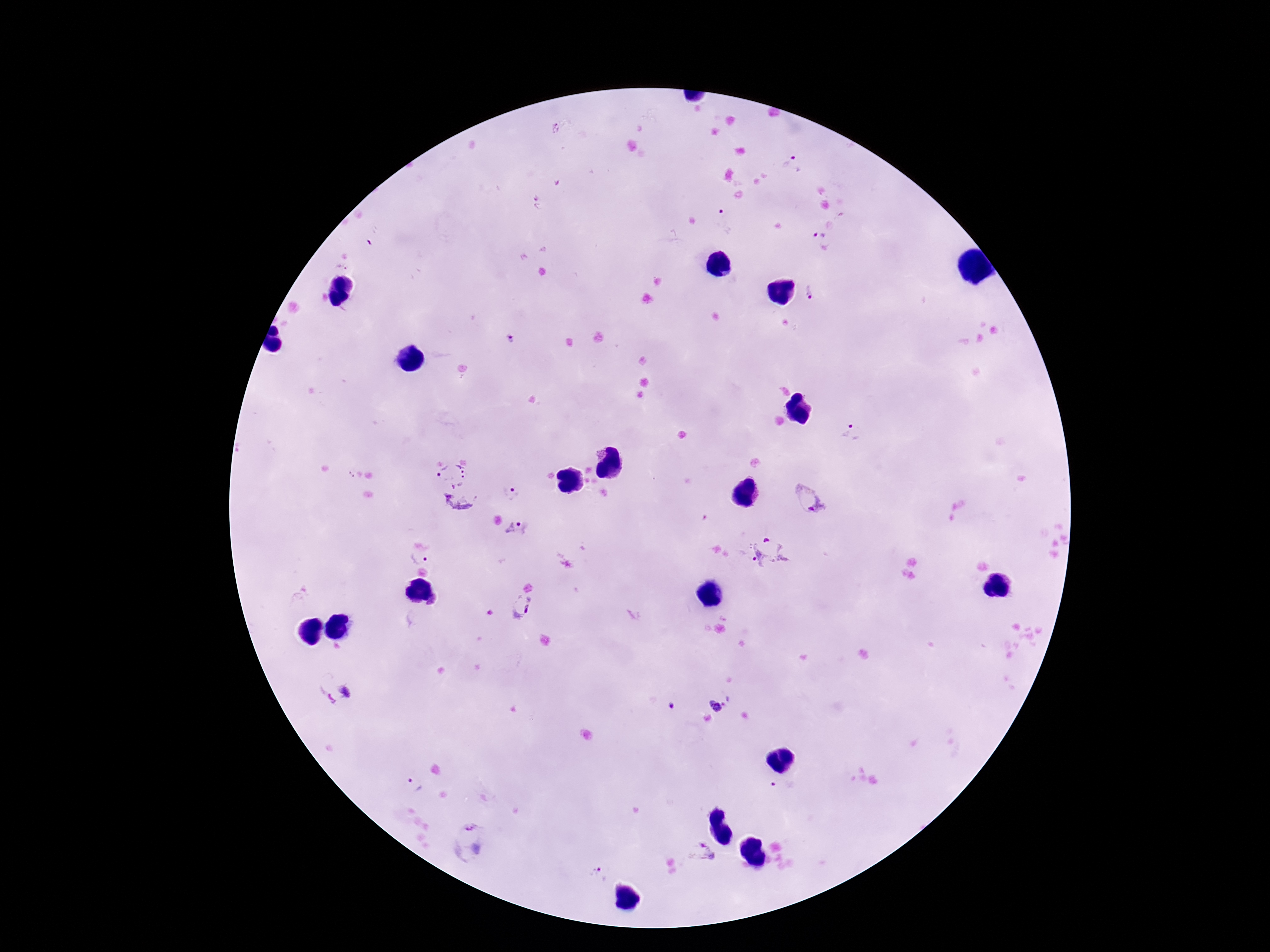
patient malaria status = positive
image size = 1270×952 pixels
magnification = 100x
field of view = single
stain = Giemsa
capture = smartphone camera through the microscope eyepiece
Plasmodium parasite locations = approximate object centers, in pixels from the top-left corner: (x=794, y=165), (x=725, y=221), (x=818, y=235), (x=811, y=293), (x=510, y=339), (x=853, y=433), (x=451, y=472), (x=510, y=494), (x=809, y=500), (x=459, y=504), (x=518, y=530), (x=767, y=552), (x=419, y=558), (x=522, y=606), (x=337, y=698), (x=723, y=700), (x=672, y=705), (x=411, y=787), (x=783, y=790), (x=471, y=842), (x=701, y=852), (x=598, y=875)
preparation = thick blood smear